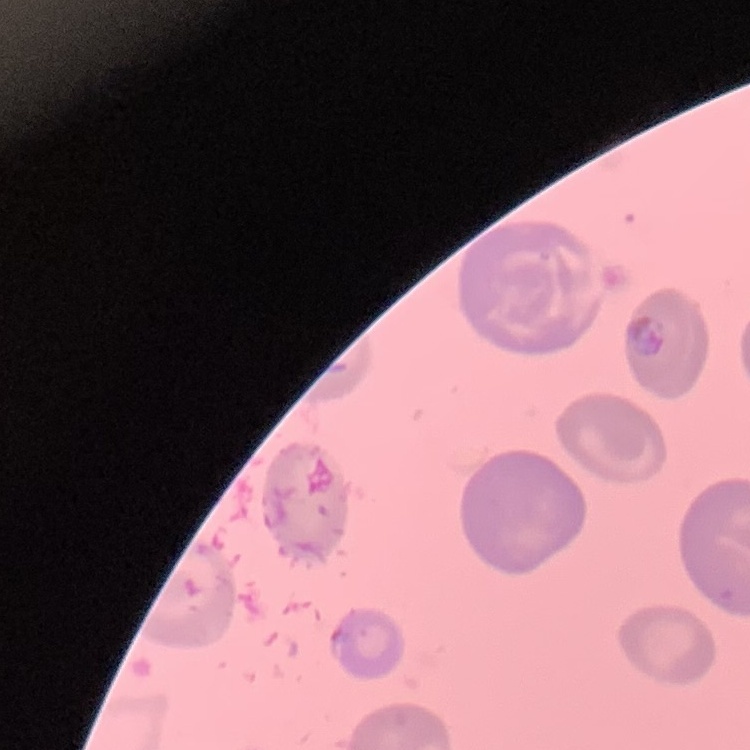
Summary:
  - Erythrocyte morphology: no rouleaux formation
  - Image type: one tile cut from a larger photomicrograph
  - Stain: Field's or Giemsa
  - Preparation: thin peripheral smear